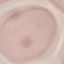
result = no malaria parasites detected
capture = smartphone camera at the microscope eyepiece
preparation = thin smear
stain = Giemsa
image type = automatically extracted cell patch, resized to 64 × 64 pixels